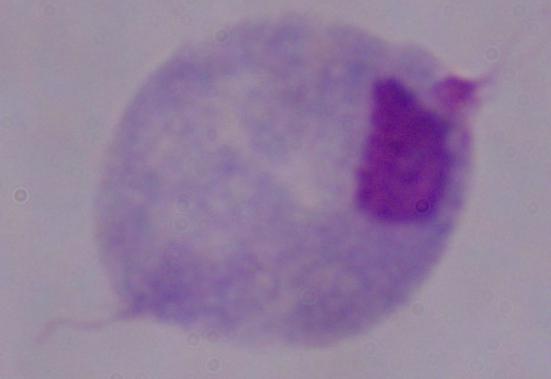

Summary:
  - Modality: photomicrograph
  - Magnification: 1000x
  - Identification: trichomonad